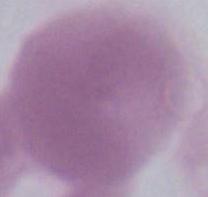 Captured at 1000x magnification. Photomicrograph. A red blood cell is seen.